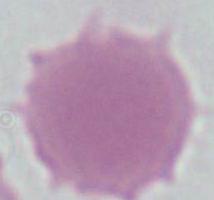

modality: micrograph
magnification: 1000x
identification: erythrocyte